Classify this cell by malaria status.
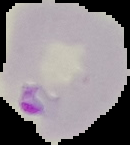
Parasitized.

Summary:
  - Image size: 130×145 pixels
  - Image type: segmented cell region with the area outside set to black
  - Preparation: thin blood smear